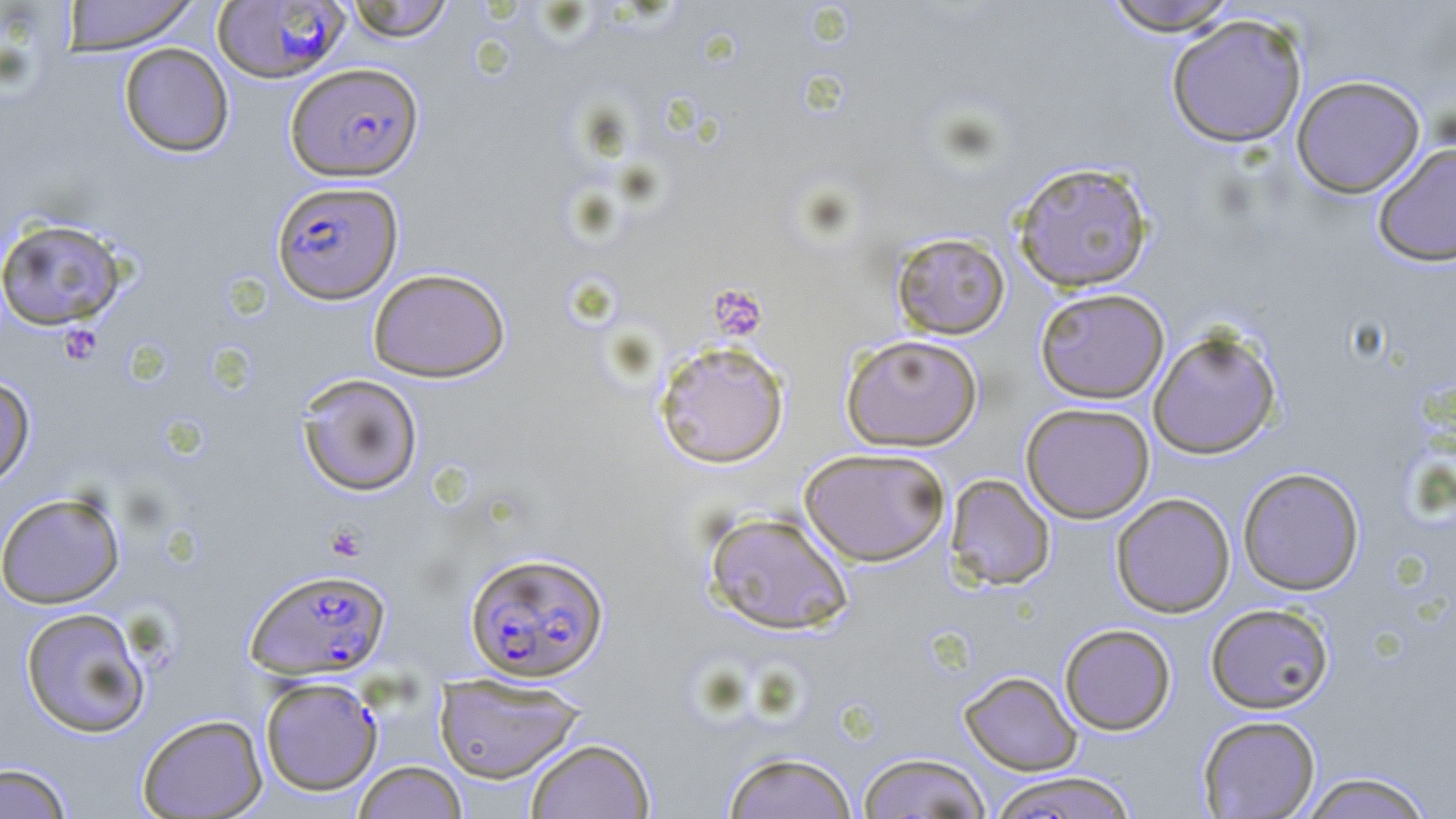

Summary:
  - Coordinate format: approximate bounding boxes as (x1,y1)-(x2,y2) corner pairs in pixels
  - Plasmodium falciparum-infected red blood cell locations (subset): (211,1)-(351,83), (286,62)-(423,181), (271,181)-(403,304), (463,550)-(610,682), (245,568)-(392,679)
  - Platelet locations: (708,284)-(768,341), (59,324)-(102,363), (325,524)-(367,561)
  - Uninfected red blood cell locations (subset): (61,0)-(201,55), (342,0)-(457,42), (1099,0)-(1242,36), (1165,13)-(1308,148), (118,42)-(234,158), (1291,75)-(1426,197), (1372,142)-(1456,267), (1012,161)-(1154,293), (0,218)-(128,331), (890,231)-(1011,340), (368,268)-(511,382), (1034,287)-(1170,404), (1147,328)-(1282,459), (840,334)-(983,452), (653,340)-(791,469), (296,373)-(424,496), (0,374)-(36,489), (1020,402)-(1155,523), (799,447)-(951,567), (1237,467)-(1365,595), (945,474)-(1056,591), (0,491)-(126,608), (1110,492)-(1236,618), (704,511)-(854,636), (1205,603)-(1334,714), (19,607)-(151,738), (1059,624)-(1177,735), (958,671)-(1082,775), (433,672)-(586,784), (137,713)-(267,818), (1197,714)-(1321,818), (524,738)-(655,818), (721,750)-(858,819), (857,752)-(992,818), (353,760)-(468,819), (1,762)-(73,818), (985,770)-(1139,819), (1297,771)-(1435,819)
  - Slide-level diagnosis: Plasmodium falciparum
  - Modality: optical microscopy
  - Image size: 1456×819 pixels
  - Field of view: one of a larger specimen
  - Magnification: 1000x
  - Stain: May-Grünwald-Giemsa
  - Preparation: thin blood smear